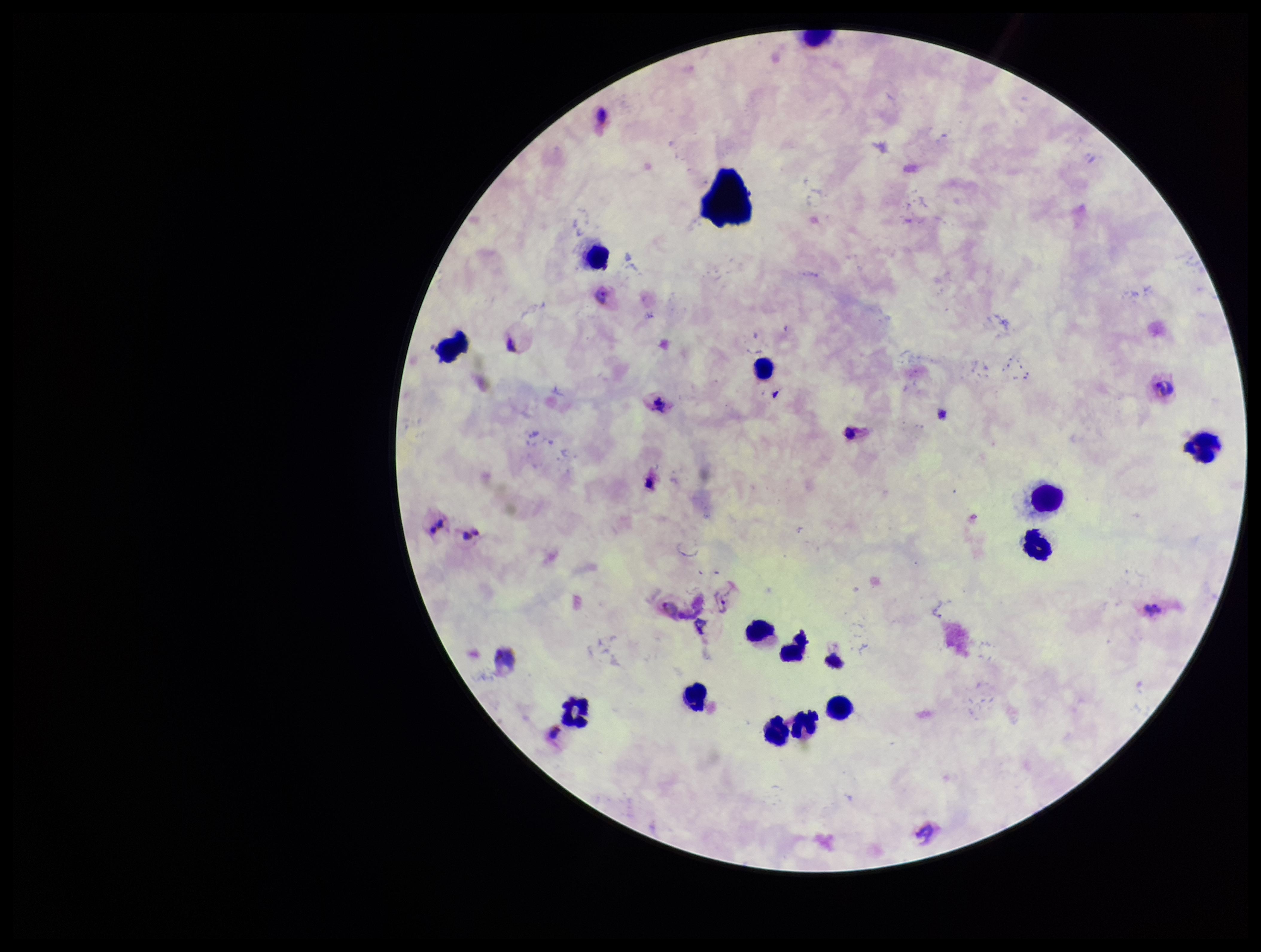

species reported for this patient = Plasmodium vivax
capture = smartphone photograph through the microscope eyepiece
leukocyte count = 13
parasite count = 1
patient malaria status = positive
image size = 1261×952 pixels
stain = Giemsa
Plasmodium parasites = seen
field of view = single
preparation = thick smear